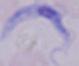
identification = trypanosome
magnification = 1000x
modality = micrograph